Classify this cell by malaria status.
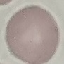

It is uninfected.

preparation = thin blood smear
stain = Giemsa
image type = cell patch, automatically extracted from a larger field of view and resized to 64 × 64 pixels
capture = smartphone through the microscope eyepiece